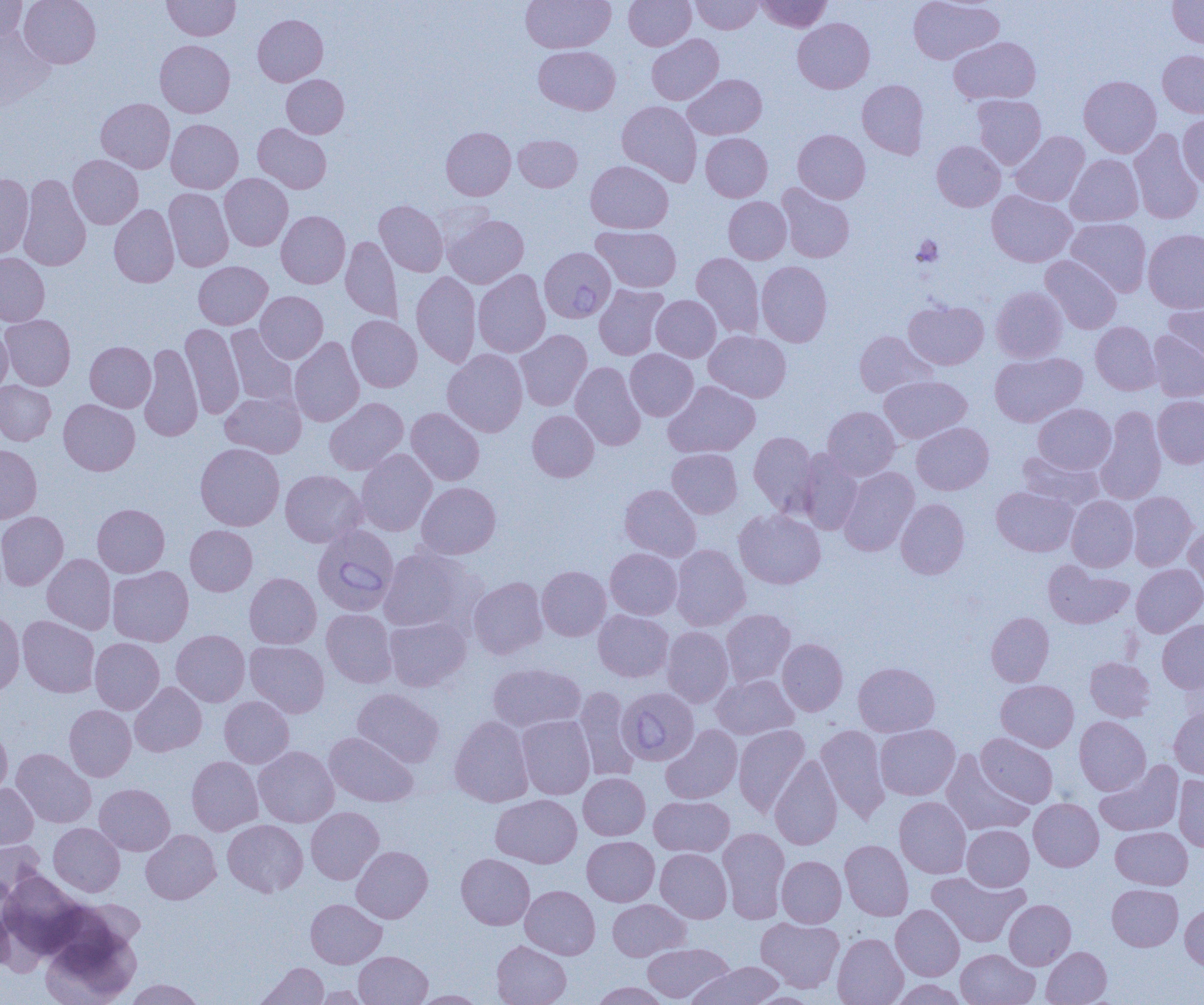 Approximate bounding boxes as [x1, y1, x2, y2] in pixels. Uninfected red blood cell locations: [0, 0, 27, 41], [19, 0, 101, 68], [522, 0, 615, 52], [624, 0, 696, 50], [690, 0, 762, 34], [756, 0, 832, 32], [907, 0, 1004, 65], [1168, 0, 1204, 47], [162, 1, 240, 40], [253, 14, 328, 86], [793, 18, 874, 93], [0, 29, 55, 111], [646, 34, 723, 105], [949, 36, 1041, 105], [155, 40, 235, 118], [534, 45, 620, 114], [1158, 50, 1204, 118], [281, 74, 348, 138], [683, 74, 767, 140], [1079, 75, 1161, 157], [857, 79, 928, 158], [972, 94, 1046, 169], [96, 98, 175, 173], [617, 100, 702, 186], [1177, 114, 1204, 188], [166, 119, 243, 193], [253, 123, 331, 193], [441, 127, 515, 200], [1129, 128, 1203, 224], [793, 129, 870, 203], [1010, 131, 1089, 206], [701, 133, 772, 202], [514, 135, 582, 191], [932, 140, 1005, 211], [68, 154, 143, 229], [1066, 154, 1143, 226], [585, 160, 673, 233], [219, 173, 293, 251], [0, 174, 33, 258], [18, 174, 91, 271], [776, 184, 855, 262], [163, 188, 234, 271], [987, 190, 1077, 267], [723, 197, 791, 263], [375, 200, 448, 276], [109, 204, 179, 287], [276, 211, 350, 288], [443, 213, 529, 288], [1065, 218, 1151, 296], [592, 225, 681, 293], [1143, 229, 1204, 313], [341, 236, 403, 323], [691, 252, 764, 338], [0, 253, 49, 326], [1041, 255, 1122, 334], [193, 261, 272, 329], [756, 261, 832, 347], [473, 269, 550, 358], [412, 271, 481, 368], [594, 284, 668, 360], [991, 286, 1067, 362], [255, 291, 328, 363], [651, 295, 721, 362], [1163, 297, 1204, 371], [903, 300, 989, 369], [1, 314, 75, 390], [347, 315, 422, 392], [1090, 321, 1161, 395], [180, 323, 244, 418], [225, 325, 298, 408], [0, 326, 12, 395], [514, 329, 592, 411], [704, 330, 791, 402], [1148, 330, 1204, 401], [854, 331, 937, 397], [289, 337, 364, 427], [85, 341, 156, 412], [138, 343, 203, 441], [442, 349, 528, 437], [625, 349, 698, 421], [989, 352, 1087, 427], [570, 362, 646, 450], [879, 376, 972, 443], [0, 380, 55, 445], [663, 381, 760, 458], [220, 391, 306, 458], [1153, 395, 1204, 468], [324, 397, 408, 475], [58, 399, 140, 475], [1033, 403, 1116, 474], [823, 406, 900, 480], [1096, 406, 1166, 505], [406, 407, 484, 485], [527, 410, 599, 482], [912, 422, 993, 495], [749, 432, 819, 516], [195, 442, 285, 530], [0, 445, 42, 524], [667, 448, 742, 518], [356, 449, 437, 536], [798, 449, 863, 534], [1017, 451, 1103, 509], [839, 467, 919, 555], [280, 470, 366, 547], [416, 482, 501, 559], [620, 484, 701, 561], [991, 486, 1078, 556], [1126, 491, 1198, 571], [1066, 496, 1138, 572], [896, 498, 969, 579], [92, 504, 169, 577], [734, 509, 826, 589], [0, 511, 68, 590], [1183, 522, 1204, 599], [185, 525, 257, 596], [671, 544, 750, 631], [377, 547, 477, 632], [605, 548, 682, 619], [42, 554, 116, 634], [1043, 561, 1134, 628], [1131, 563, 1204, 637], [537, 565, 611, 641], [107, 566, 194, 647], [244, 573, 321, 649], [468, 576, 547, 659], [0, 609, 24, 696], [322, 609, 398, 687], [593, 609, 673, 682], [721, 609, 795, 687], [986, 612, 1054, 686], [18, 615, 99, 697], [384, 615, 471, 692], [1157, 620, 1204, 694], [662, 626, 733, 707], [171, 630, 250, 706], [90, 638, 164, 714], [777, 638, 847, 716], [245, 641, 329, 717], [1085, 657, 1154, 721], [853, 662, 940, 736], [487, 663, 585, 733], [712, 674, 798, 739], [996, 679, 1079, 751], [130, 682, 207, 757], [573, 686, 640, 781], [352, 688, 444, 767], [219, 696, 294, 767], [64, 704, 136, 781], [1169, 707, 1204, 779], [449, 715, 533, 806], [516, 715, 595, 799], [1074, 716, 1150, 795], [733, 724, 810, 816], [874, 724, 960, 800], [661, 725, 742, 804], [815, 725, 890, 823], [0, 726, 12, 798], [324, 732, 418, 807], [976, 733, 1058, 807], [253, 746, 339, 827], [11, 748, 96, 828], [941, 751, 1034, 836], [769, 755, 843, 850], [186, 756, 263, 835], [1095, 761, 1184, 836], [578, 773, 650, 840], [1174, 774, 1204, 851], [0, 783, 38, 849], [94, 783, 175, 855], [491, 794, 582, 868], [649, 796, 734, 857], [894, 796, 971, 878], [1029, 798, 1103, 871], [306, 807, 384, 884], [223, 819, 308, 896], [49, 823, 124, 896], [962, 824, 1034, 891], [1111, 826, 1192, 889], [718, 827, 790, 923], [141, 829, 221, 904], [582, 836, 659, 906], [0, 840, 45, 901], [840, 840, 913, 920], [352, 846, 432, 923], [655, 848, 731, 923], [456, 853, 535, 930], [776, 856, 846, 927], [1, 871, 88, 957], [927, 871, 1029, 947], [1107, 884, 1183, 951], [520, 885, 600, 959], [0, 887, 14, 975], [305, 898, 386, 968], [607, 899, 690, 961], [1004, 899, 1075, 970], [1180, 904, 1204, 970], [891, 905, 964, 980], [756, 917, 844, 992], [41, 922, 141, 1005], [832, 933, 908, 1005], [491, 940, 571, 1005], [642, 942, 732, 1002], [1041, 946, 1111, 1005], [956, 948, 1039, 1005], [354, 951, 432, 1005], [255, 962, 328, 1005], [689, 962, 785, 1005], [124, 979, 206, 1004], [892, 979, 966, 1005], [590, 982, 672, 1004], [311, 985, 370, 1004], [412, 990, 488, 1004]. Platelet locations: [911, 236, 943, 267]. Babesia divergens-infected red blood cell locations: [539, 246, 615, 324], [312, 524, 399, 616], [621, 687, 700, 761]. Slide-level diagnosis: Babesia divergens. One field of a larger specimen. Image is 1204×1005 pixels. Light microscopy. Thin blood film. Captured at 1000x magnification.